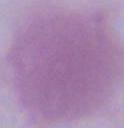
magnification = 1000x
modality = photomicrograph
identification = erythrocyte